Classify this cell by malaria status.
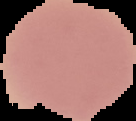
It is uninfected.

The area outside the segmented cell region is set to black. Image is 136×121 pixels. From a thin blood smear.